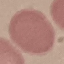
Summary:
  - Result: no malaria parasites seen
  - Image type: cell patch, automatically extracted from a larger field of view and resized to 64 × 64 pixels
  - Stain: Giemsa
  - Capture: smartphone camera at the microscope eyepiece
  - Preparation: thin blood film